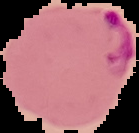 Result: Plasmodium parasites identified. From a thin blood film. Cell region segmented out of the field of view; the surrounding area is masked to black. Image is 139×133 pixels.